Locate every Plasmodium parasite.
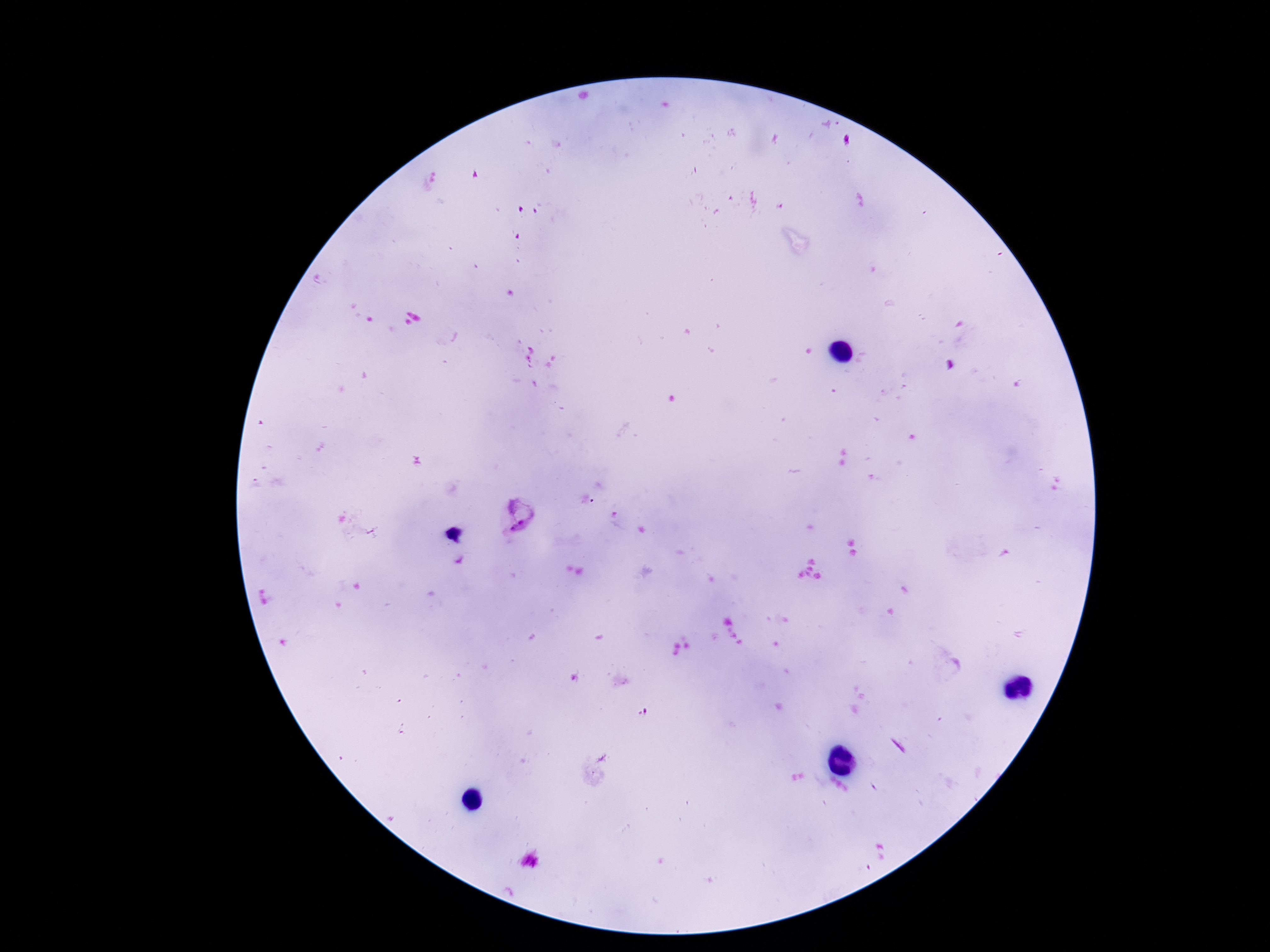

Approximate centers as (x, y) in pixels.
Plasmodium parasites: (518, 518).

Giemsa-stained preparation. One field from this slide. Photographed through the microscope eyepiece with a smartphone camera. Patient malaria status: positive. 100x magnification. Thick blood film. Image is 1270×952 pixels.